Assess this cell for malaria.
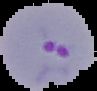

Parasitized.

Summary:
  - Preparation: thin blood smear
  - Image size: 97×91 pixels
  - Image type: cell region segmented out of the field of view; surrounding area masked to black